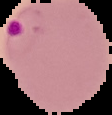
preparation = thin blood smear
image type = segmented cell region on a black background
result = malaria parasites detected
image size = 112×115 pixels